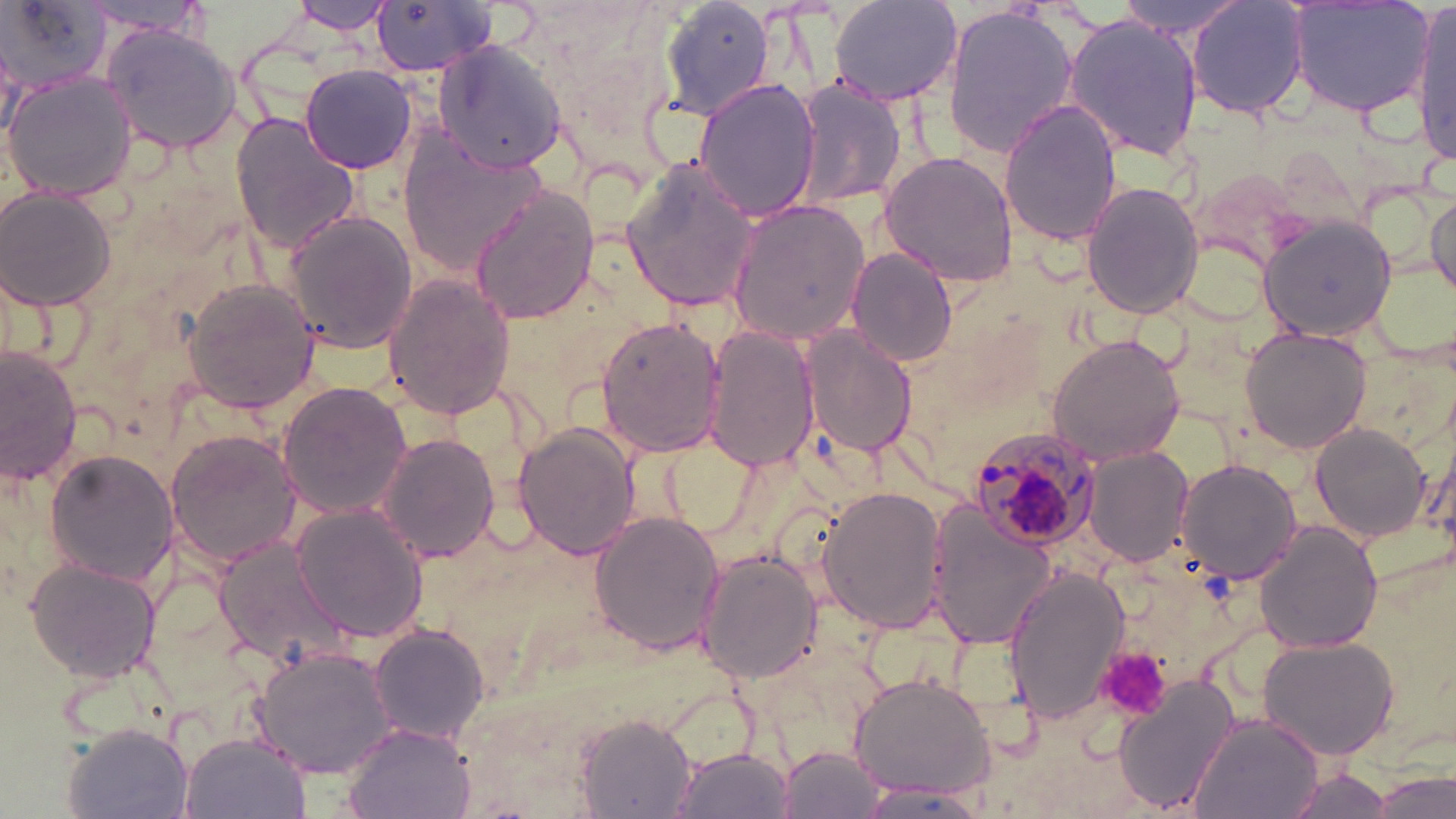

slide-level diagnosis = Plasmodium malariae
magnification = 1000x
preparation = thin blood film
image size = 1456×819 pixels
modality = optical microscopy
stain = May-Grünwald-Giemsa
platelet locations = approximate bounding boxes as (x1, y1, x2, y2) in pixels: (1094, 644, 1172, 722)
uninfected red blood cell locations = approximate bounding boxes as (x1, y1, x2, y2) in pixels: (1, 0, 112, 95), (366, 0, 497, 80), (657, 0, 777, 121), (828, 0, 964, 108), (1113, 0, 1244, 38), (1187, 0, 1311, 122), (1287, 0, 1435, 117), (284, 1, 395, 35), (73, 3, 212, 37), (941, 5, 1080, 158), (1411, 6, 1455, 161), (1062, 12, 1206, 163), (101, 22, 248, 154), (431, 39, 569, 174), (298, 63, 418, 172), (5, 71, 137, 200), (693, 78, 821, 223), (792, 80, 908, 211), (999, 100, 1123, 249), (228, 112, 362, 253), (399, 132, 552, 274), (877, 149, 1022, 289), (620, 160, 760, 313), (1080, 178, 1204, 320), (468, 186, 596, 326), (2, 187, 120, 311), (1426, 194, 1456, 297), (725, 197, 871, 348), (283, 210, 421, 355), (1258, 210, 1401, 342), (847, 248, 958, 367), (826, 261, 946, 434), (382, 274, 517, 419), (179, 276, 322, 415), (597, 313, 728, 458), (702, 324, 819, 473), (800, 325, 918, 458), (1238, 325, 1373, 454), (1046, 331, 1190, 466), (0, 347, 82, 491), (275, 379, 412, 521), (1308, 422, 1435, 544), (511, 423, 640, 561), (163, 429, 302, 569), (374, 430, 501, 565), (1082, 446, 1195, 567), (41, 447, 185, 591), (1173, 458, 1301, 589), (818, 485, 950, 633), (925, 503, 1058, 649), (291, 504, 429, 642), (588, 508, 724, 657), (1253, 519, 1387, 654), (1339, 538, 1456, 758), (211, 540, 353, 668), (696, 549, 821, 684), (24, 559, 164, 681), (1003, 569, 1130, 722), (367, 623, 490, 746), (1258, 637, 1398, 760), (254, 646, 398, 779), (847, 672, 996, 800), (1111, 673, 1240, 817), (576, 710, 698, 816), (1189, 713, 1323, 819), (339, 721, 478, 819), (63, 723, 195, 819), (181, 734, 307, 817), (777, 745, 887, 819), (669, 746, 796, 819), (1374, 765, 1455, 819), (1282, 767, 1392, 818), (859, 785, 989, 815)
Plasmodium malariae-infected red blood cell locations = approximate bounding boxes as (x1, y1, x2, y2) in pixels: (969, 426, 1104, 550)
field of view = one of a larger specimen